Locate every Plasmodium parasite.
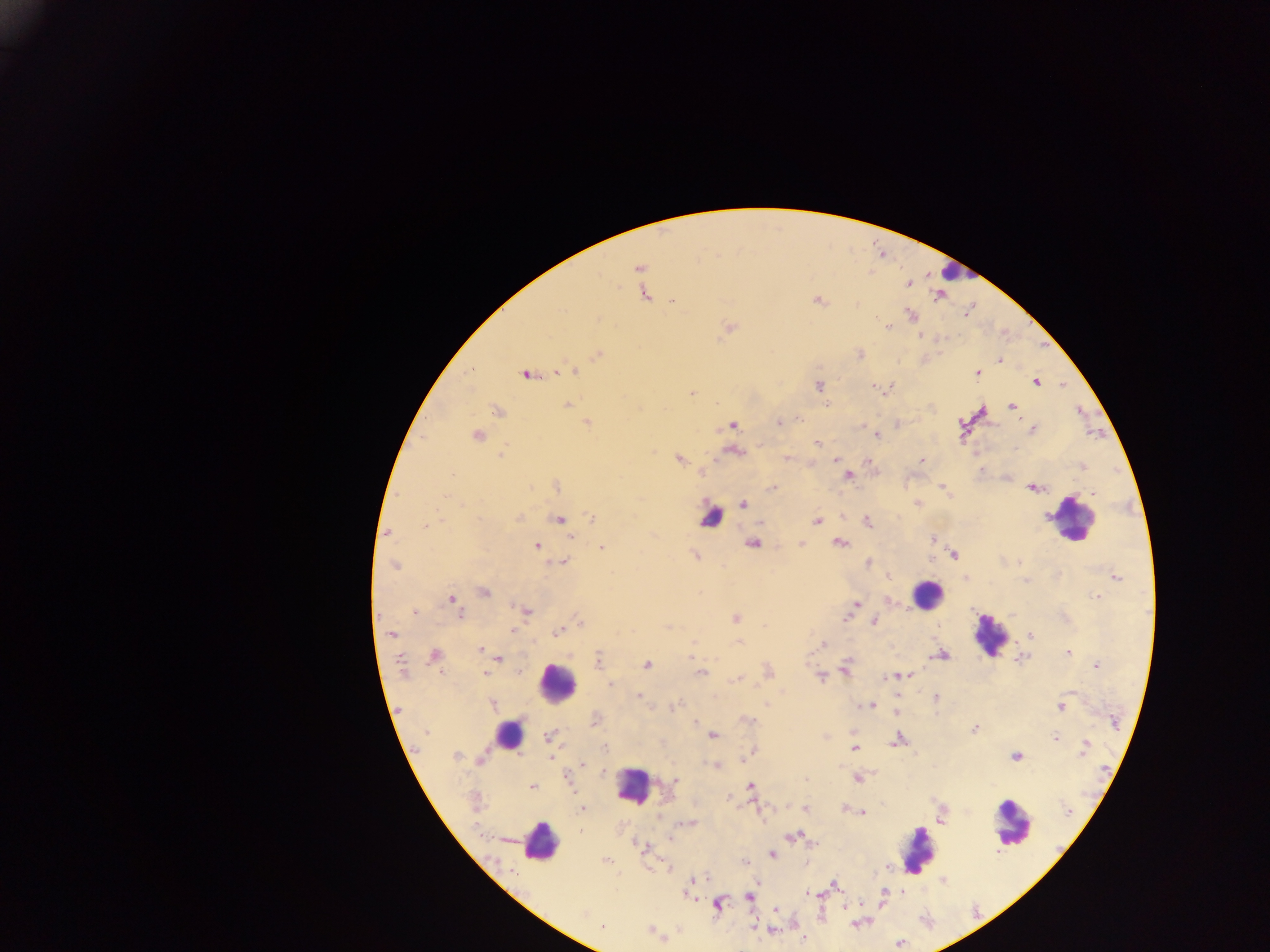
Approximate centers as (x, y) in pixels.
Plasmodium parasites: (639, 268), (907, 282), (645, 294), (940, 294), (673, 299), (818, 300), (910, 315), (728, 327), (887, 327), (919, 335), (860, 353), (597, 354), (999, 359), (470, 369), (571, 370), (562, 371), (978, 372), (526, 374), (1036, 381), (1062, 384), (819, 385), (885, 389), (691, 392), (567, 405), (827, 405), (1012, 406), (496, 410), (587, 422), (779, 422), (898, 423), (732, 425), (861, 425), (1032, 429), (476, 435), (876, 435), (817, 443), (734, 450), (501, 453), (678, 458), (787, 458), (836, 458), (923, 459), (868, 461), (812, 463), (1082, 467), (700, 473), (847, 475), (556, 486), (941, 487), (772, 488), (1033, 488), (917, 503), (741, 504), (841, 516), (518, 518), (591, 518), (558, 519), (817, 520), (760, 521), (866, 521), (424, 526), (387, 533), (570, 535), (932, 539), (752, 542), (839, 543), (801, 544), (536, 546), (602, 547), (954, 554), (694, 555), (562, 562), (867, 564), (396, 565), (886, 575), (1115, 576), (965, 577), (1026, 580), (484, 592), (1096, 595), (450, 599), (886, 601), (854, 607), (526, 612), (415, 613), (457, 614), (735, 617), (873, 620), (580, 621), (668, 627), (513, 629), (558, 631), (391, 635), (1029, 636), (739, 641), (821, 644), (480, 648), (1068, 652), (941, 654), (434, 655), (692, 655), (1021, 657), (499, 659), (598, 661), (646, 664), (1096, 664), (844, 668), (520, 671), (701, 671), (767, 671), (486, 673), (904, 675), (897, 676), (820, 677), (739, 679), (610, 684), (637, 696), (935, 697), (766, 703), (492, 704), (870, 705), (673, 707), (1060, 707), (895, 711), (595, 719), (747, 719), (695, 722), (973, 729), (852, 733), (549, 736), (712, 736), (825, 736), (1055, 738), (896, 739), (1085, 746), (604, 747), (854, 748), (753, 751), (455, 755), (746, 755), (1015, 755), (550, 756), (742, 758), (480, 760), (582, 765), (716, 766), (567, 778), (857, 778), (804, 779), (675, 780), (531, 786), (750, 787), (728, 798), (844, 808), (582, 809), (806, 809), (1067, 811), (862, 813), (941, 815), (690, 823), (794, 836), (669, 837), (645, 848), (772, 854), (606, 860), (743, 860), (667, 867), (886, 868), (693, 880), (757, 880), (942, 880), (835, 885), (690, 886), (688, 893), (806, 893), (812, 893), (821, 893), (883, 893), (749, 897), (717, 904), (845, 906), (776, 908), (854, 922), (601, 927), (753, 927), (773, 930), (651, 931), (803, 941).

Summary:
  - Leukocyte locations: (955, 271), (711, 516), (1073, 518), (927, 594), (990, 636), (557, 683), (508, 734), (633, 786), (1012, 822), (540, 841), (917, 851)
  - Image size: 1270×952 pixels
  - Capture: mobile-phone photograph through a microscope
  - Country: Ghana
  - Field of view: single
  - Preparation: thick blood smear